Report the malaria status of this cell.
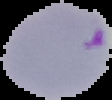

It is parasitized.

Image is 112×100 pixels. The area outside the segmented cell region is set to black. From a thin blood smear.